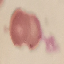
malaria status = uninfected
stain = Giemsa
capture = smartphone camera at the microscope eyepiece
preparation = thin blood smear
image type = cell patch, automatically extracted from a larger field of view and resized to 64 × 64 pixels